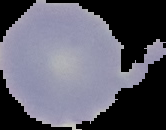
preparation = thin blood smear
image type = segmented cell region with the area outside set to black
result = no Plasmodium parasites seen
image size = 166×130 pixels